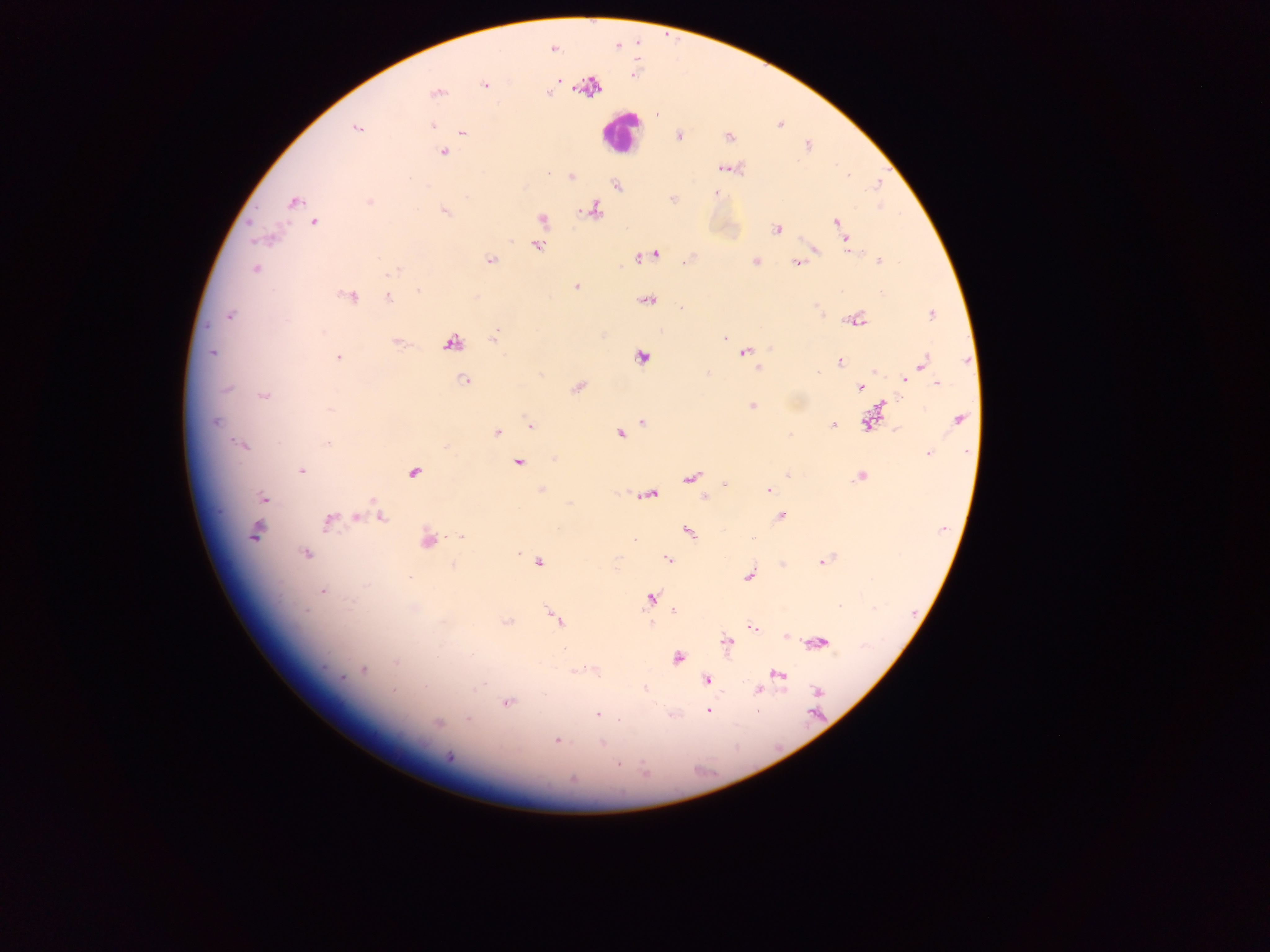

{
  "image_size": "1270×952 pixels",
  "field_of_view": "single",
  "leukocyte_locations": "approximate centers as (x, y) in pixels: (619, 131)",
  "plasmodium_parasite_locations": "approximate centers as (x, y) in pixels: (553, 49), (558, 80), (485, 84), (550, 93), (435, 94), (657, 114), (433, 125), (356, 128), (462, 133), (679, 136), (728, 137), (442, 152), (726, 168), (571, 177), (616, 185), (717, 193), (293, 202), (369, 202), (594, 210), (444, 211), (542, 220), (836, 222), (315, 223), (776, 229), (846, 239), (537, 246), (850, 252), (655, 253), (639, 257), (490, 260), (879, 261), (684, 262), (755, 262), (795, 263), (255, 270), (395, 270), (575, 287), (419, 292), (350, 296), (388, 297), (648, 301), (681, 308), (931, 314), (230, 316), (856, 320), (495, 336), (725, 338), (397, 342), (453, 343), (745, 351), (212, 353), (338, 357), (641, 357), (839, 362), (923, 362), (759, 367), (874, 371), (818, 372), (904, 379), (465, 381), (937, 384), (577, 387), (227, 388), (860, 388), (263, 395), (881, 404), (752, 406), (330, 410), (958, 419), (214, 421), (643, 421), (868, 421), (530, 426), (833, 426), (896, 429), (497, 432), (620, 434), (328, 443), (242, 446), (928, 453), (519, 462), (302, 470), (413, 473), (787, 475), (860, 476), (691, 478), (725, 484), (541, 490), (769, 490), (697, 493), (651, 495), (704, 496), (263, 498), (374, 502), (780, 516), (357, 517), (381, 517), (328, 522), (689, 531), (255, 533), (461, 536), (753, 538), (428, 540), (635, 540), (306, 554), (518, 554), (668, 559), (823, 561), (539, 562), (782, 564), (453, 565), (748, 576), (410, 578), (322, 591), (651, 597), (840, 606), (413, 608), (674, 610), (555, 618), (444, 621), (507, 622), (752, 627), (787, 635), (727, 642), (821, 642), (677, 658), (396, 662), (363, 670), (778, 674), (706, 680), (480, 687), (645, 689), (758, 689), (393, 690), (817, 692), (507, 702), (708, 711), (597, 714), (469, 720), (437, 723), (557, 740), (603, 743), (450, 756), (618, 764), (573, 778)",
  "capture": "mobile-phone photograph through a microscope",
  "preparation": "thick blood film",
  "country": "Ghana"
}